Give the extent of all uninfected red blood cells.
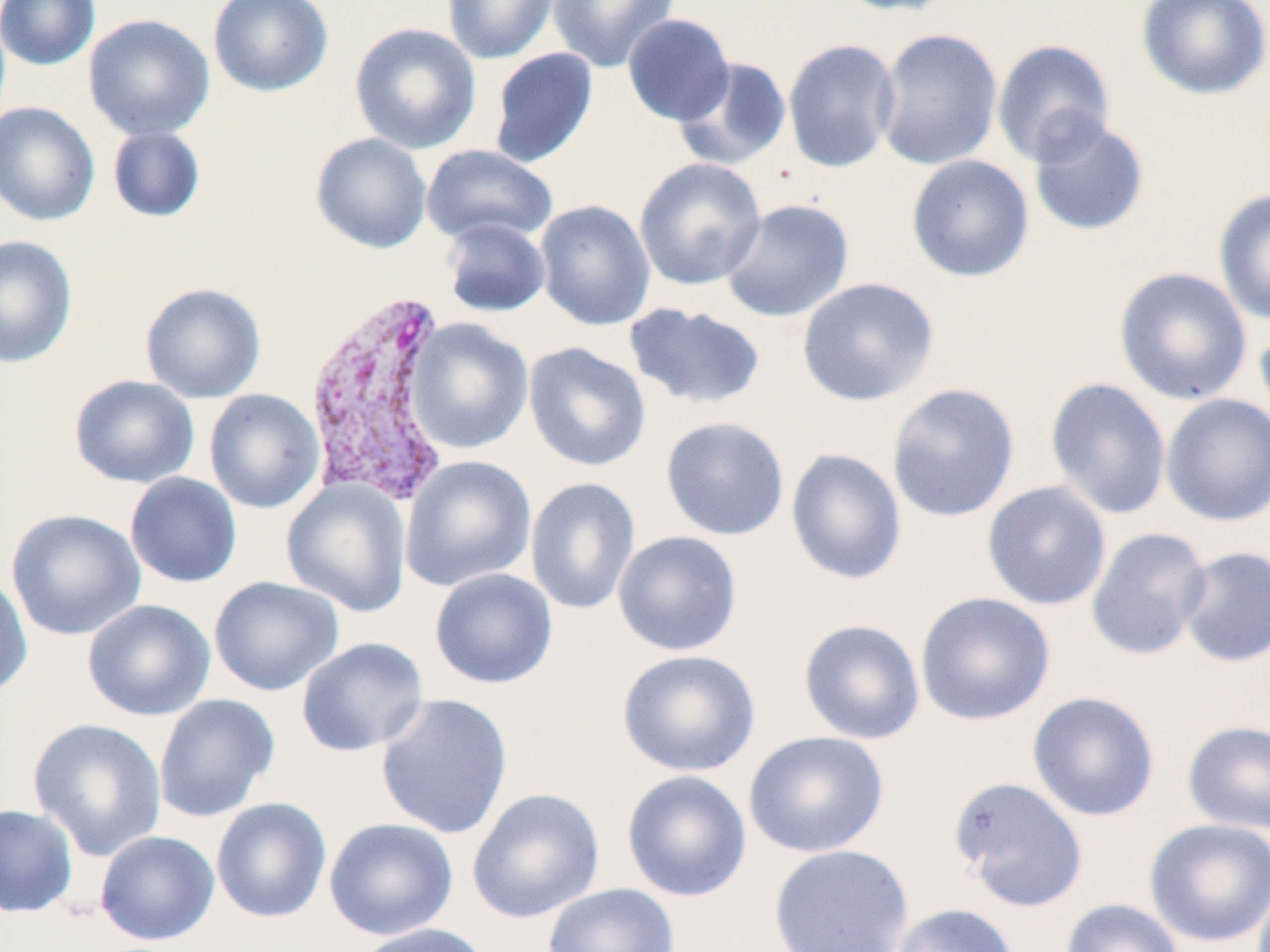

Approximate bounding boxes as [x1, y1, x2, y2] in pixels.
Uninfected red blood cells: [0, 0, 101, 71], [207, 0, 333, 97], [442, 0, 559, 64], [547, 0, 680, 73], [832, 0, 962, 18], [1136, 0, 1270, 101], [82, 13, 215, 141], [622, 13, 735, 126], [349, 22, 482, 154], [875, 28, 1003, 171], [782, 38, 902, 173], [991, 38, 1116, 166], [487, 47, 598, 169], [674, 56, 793, 170], [0, 102, 100, 226], [1027, 116, 1150, 237], [107, 125, 206, 223], [310, 132, 432, 254], [420, 144, 558, 247], [906, 154, 1034, 283], [634, 157, 767, 291], [1213, 188, 1270, 326], [719, 198, 854, 322], [534, 199, 656, 331], [440, 218, 551, 318], [0, 234, 78, 369], [1113, 267, 1252, 405], [797, 277, 939, 407], [139, 282, 266, 404], [624, 301, 766, 410], [1253, 315, 1270, 435], [404, 318, 534, 454], [523, 341, 651, 473], [69, 374, 200, 489], [1044, 377, 1172, 520], [886, 382, 1020, 523], [203, 388, 325, 514], [1160, 393, 1270, 527], [660, 416, 790, 541], [785, 447, 907, 585], [400, 455, 537, 592], [124, 472, 242, 588], [525, 476, 641, 615], [281, 479, 412, 617], [981, 480, 1112, 611], [6, 509, 145, 641], [1085, 526, 1212, 661], [612, 530, 743, 656], [1177, 545, 1269, 667], [429, 568, 558, 690], [0, 571, 33, 700], [208, 576, 344, 697], [915, 591, 1056, 726], [81, 599, 215, 721], [798, 618, 925, 745], [295, 637, 429, 757], [616, 648, 761, 777], [1027, 691, 1160, 822], [153, 693, 280, 823], [375, 693, 513, 840], [28, 718, 167, 861], [1181, 720, 1270, 834], [743, 730, 889, 858], [621, 770, 752, 902], [948, 776, 1088, 912], [467, 786, 605, 923], [211, 797, 332, 923], [0, 804, 79, 918], [323, 817, 458, 941], [1144, 817, 1270, 948], [94, 830, 220, 946], [768, 844, 914, 952], [542, 882, 680, 952], [1061, 898, 1185, 952], [890, 903, 1019, 952], [354, 922, 491, 952].

slide-level diagnosis = Plasmodium vivax
field of view = single
modality = optical microscopy
stain = May-Grünwald-Giemsa
image size = 1270×952 pixels
magnification = 1000x
Plasmodium vivax-infected red blood cell locations = approximate bounding boxes as [x1, y1, x2, y2] in pixels: [303, 286, 456, 504]
preparation = thin blood film